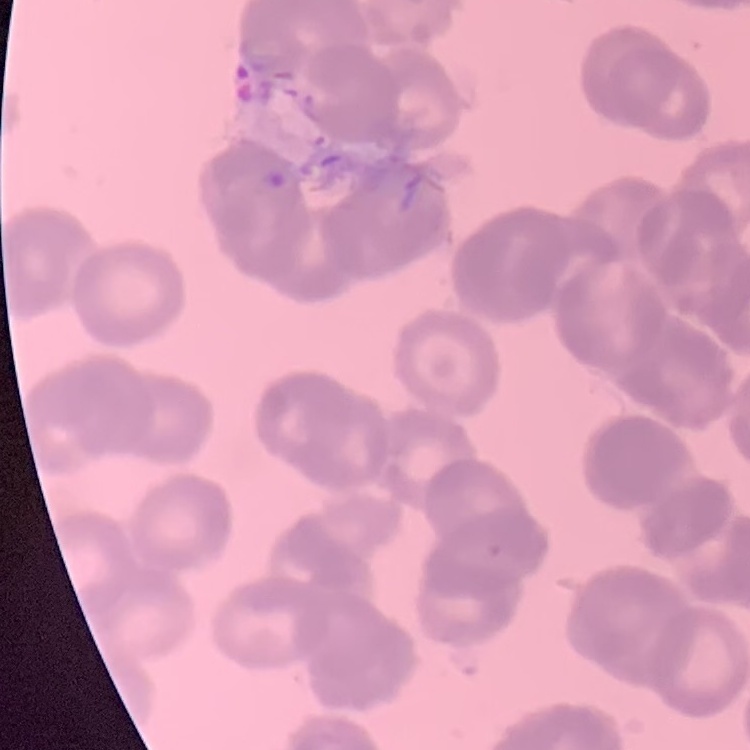

The red blood cells exhibit rouleaux formation. Thin blood film. Square crop of a larger photomicrograph. Field's or Giemsa stain.